Locate every Plasmodium falciparum parasite and give its life-cycle stage, and locate every leukocyte and any debris.
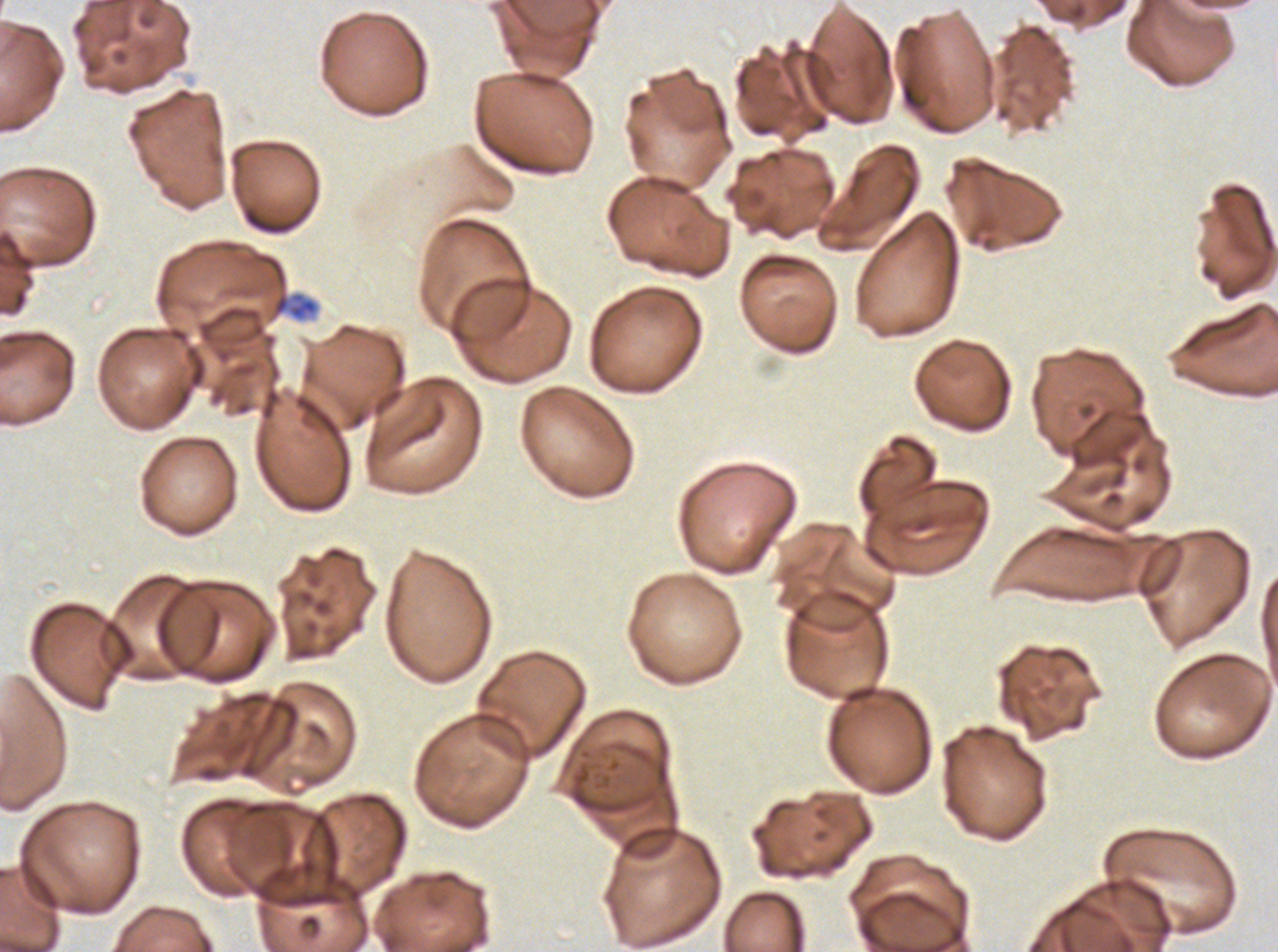

Approximate bounding boxes as (x1, y1, x2, y2) in pixels.
Debris: (274, 296, 289, 313).
No rings, late-ring/early-trophozoite forms, mid trophozoites, late trophozoites, early schizonts, late schizonts, segmenters, gametocytes, or leukocytes observed.

Summary:
  - Specimen: ex-vivo Plasmodium falciparum culture from a patient in The Gambia, grown for 24 to 48 hours
  - Preparation: thin blood film
  - Stain: Giemsa
  - Image size: 1278×952 pixels
  - Field of view: one sub-image of a larger composite